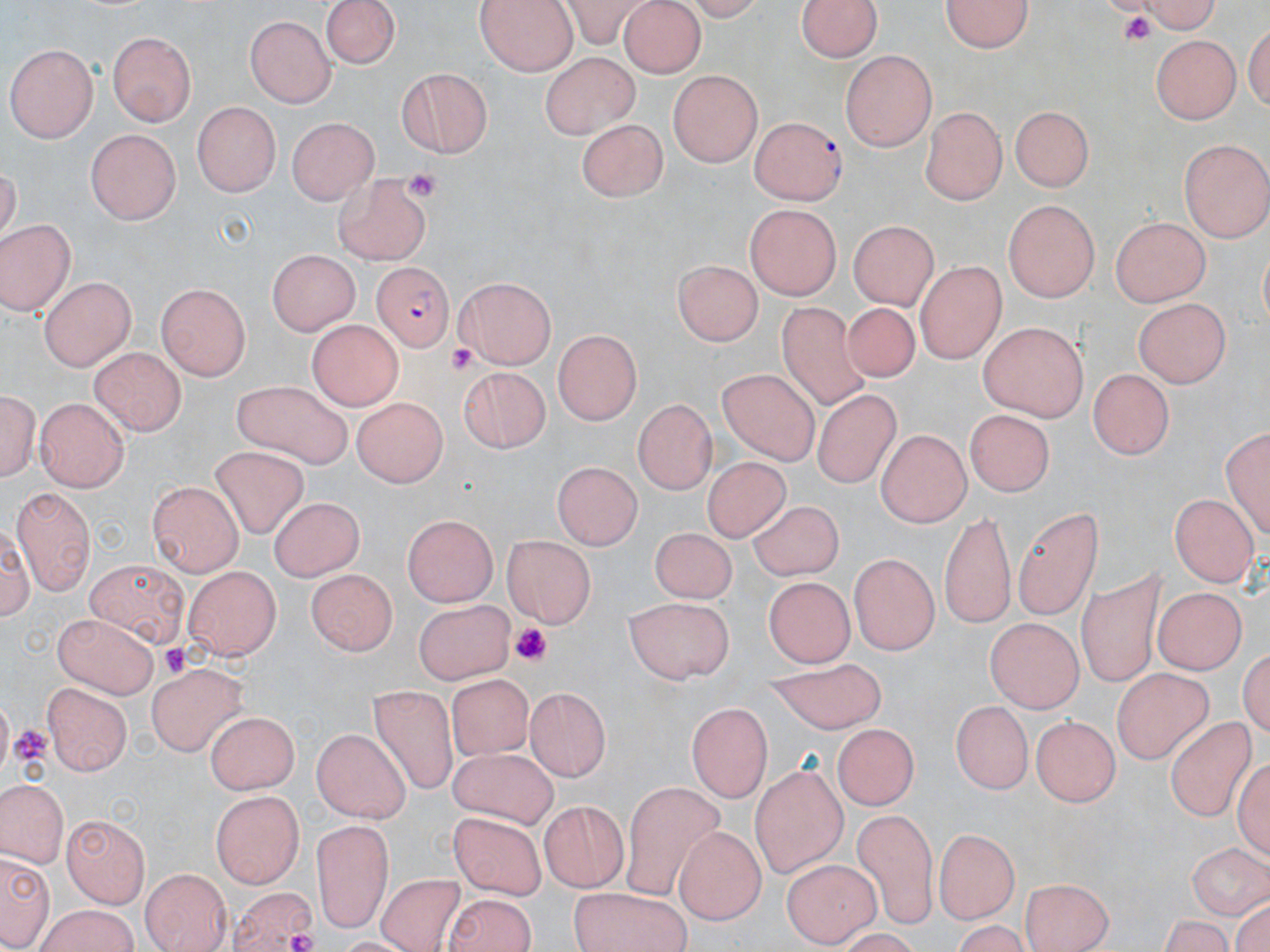

slide-level diagnosis = Plasmodium falciparum
stain = May-Grünwald-Giemsa
Plasmodium falciparum-infected red blood cell locations = approximate bounding boxes as [x1, y1, x2, y2] in pixels: [750, 116, 847, 207], [373, 262, 457, 348]
preparation = thin blood smear
uninfected red blood cell locations = approximate bounding boxes as [x1, y1, x2, y2] in pixels: [323, 0, 400, 69], [798, 0, 881, 64], [940, 0, 1040, 56], [1110, 0, 1224, 34], [479, 2, 577, 75], [619, 3, 707, 79], [246, 14, 334, 107], [105, 31, 196, 124], [1150, 35, 1243, 123], [8, 42, 101, 140], [840, 50, 937, 152], [542, 51, 641, 140], [394, 68, 494, 160], [667, 70, 765, 167], [192, 102, 282, 198], [1008, 103, 1095, 195], [920, 105, 1004, 203], [289, 116, 380, 203], [581, 116, 667, 201], [85, 130, 179, 224], [1179, 138, 1270, 239], [333, 171, 434, 264], [1002, 198, 1102, 303], [743, 203, 844, 299], [1111, 214, 1210, 308], [1, 219, 75, 319], [849, 220, 938, 310], [271, 246, 364, 333], [675, 259, 764, 345], [916, 261, 1003, 363], [39, 276, 136, 371], [454, 278, 556, 369], [155, 284, 252, 380], [1133, 297, 1229, 391], [774, 298, 875, 408], [836, 298, 925, 384], [305, 320, 403, 409], [975, 323, 1092, 421], [553, 327, 644, 422], [92, 347, 184, 437], [458, 364, 554, 451], [718, 369, 820, 464], [1085, 369, 1176, 458], [233, 379, 354, 470], [1, 383, 39, 487], [816, 389, 900, 484], [38, 395, 130, 491], [347, 396, 453, 484], [630, 403, 713, 495], [965, 408, 1058, 499], [1222, 422, 1268, 542], [873, 432, 971, 527], [210, 448, 311, 541], [700, 454, 794, 545], [554, 458, 644, 548], [147, 482, 242, 578], [11, 483, 93, 597], [1169, 492, 1255, 587], [270, 498, 363, 586], [1013, 504, 1106, 618], [746, 505, 848, 582], [940, 506, 1017, 629], [399, 515, 499, 606], [646, 528, 740, 605], [502, 535, 593, 629], [849, 555, 939, 652], [84, 560, 188, 644], [308, 563, 397, 662], [181, 564, 278, 659], [757, 566, 855, 668], [1078, 569, 1170, 684], [1154, 586, 1246, 675], [627, 595, 734, 683], [415, 604, 518, 685], [49, 613, 160, 699], [985, 618, 1086, 712], [764, 658, 888, 741], [146, 666, 248, 757], [1109, 666, 1212, 762], [449, 673, 535, 762], [44, 682, 133, 775], [369, 683, 458, 793], [519, 683, 606, 777], [949, 701, 1032, 795], [687, 702, 772, 802], [199, 707, 296, 788], [1033, 711, 1122, 804], [1166, 715, 1254, 825], [835, 722, 918, 812], [314, 731, 411, 826], [451, 751, 559, 828], [747, 761, 848, 876], [625, 776, 726, 903], [0, 779, 68, 866], [208, 792, 306, 885], [540, 801, 629, 891], [851, 806, 941, 930], [63, 815, 148, 907], [447, 815, 549, 902], [311, 816, 395, 931], [673, 825, 766, 922], [933, 826, 1019, 922], [1187, 839, 1269, 918], [1, 847, 52, 951], [785, 859, 878, 947], [140, 867, 232, 952], [377, 873, 467, 952], [1019, 878, 1115, 952], [227, 887, 319, 952], [566, 887, 692, 952], [446, 893, 543, 952], [34, 907, 143, 952], [1157, 913, 1235, 952]
image size = 1270×952 pixels
magnification = 1000x
modality = optical microscopy
platelet locations = approximate bounding boxes as [x1, y1, x2, y2] in pixels: [1118, 12, 1157, 50], [405, 170, 440, 197], [448, 344, 475, 375], [509, 621, 553, 669], [159, 641, 193, 677], [9, 725, 49, 764], [287, 929, 321, 952]
field of view = single